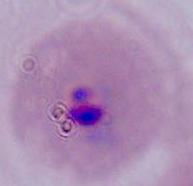

modality = photomicrograph
identification = Plasmodium
magnification = 400x or 1000x